Describe the morphology of the red blood cells.
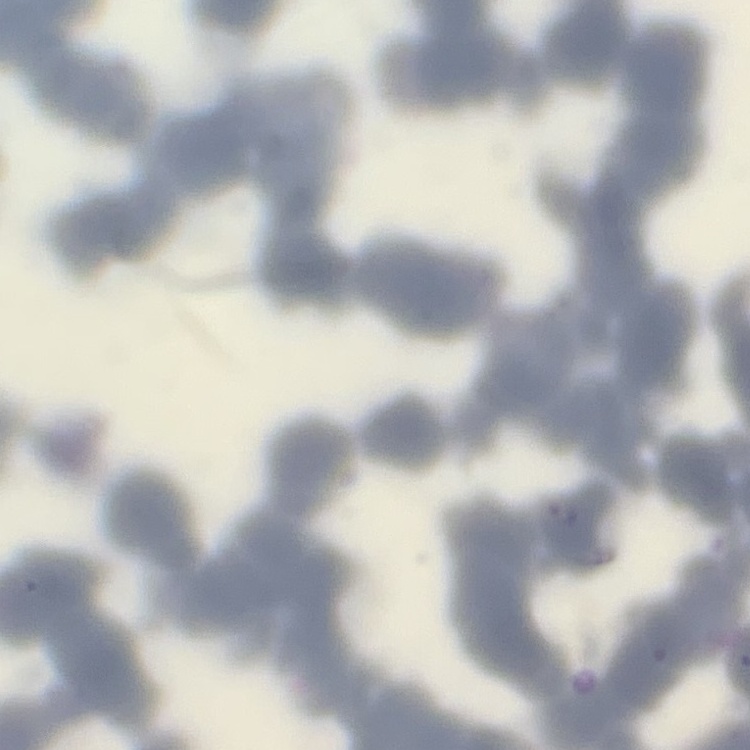
Rouleaux formation.

image type = square crop of a larger photomicrograph
stain = Field's or Giemsa
preparation = thin blood film